Assess this cell for malaria.
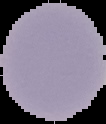

Uninfected.

Cell region segmented out of the field of view; the surrounding area is masked to black. From a thin blood smear. Image is 106×124 pixels.